Locate every Plasmodium parasite.
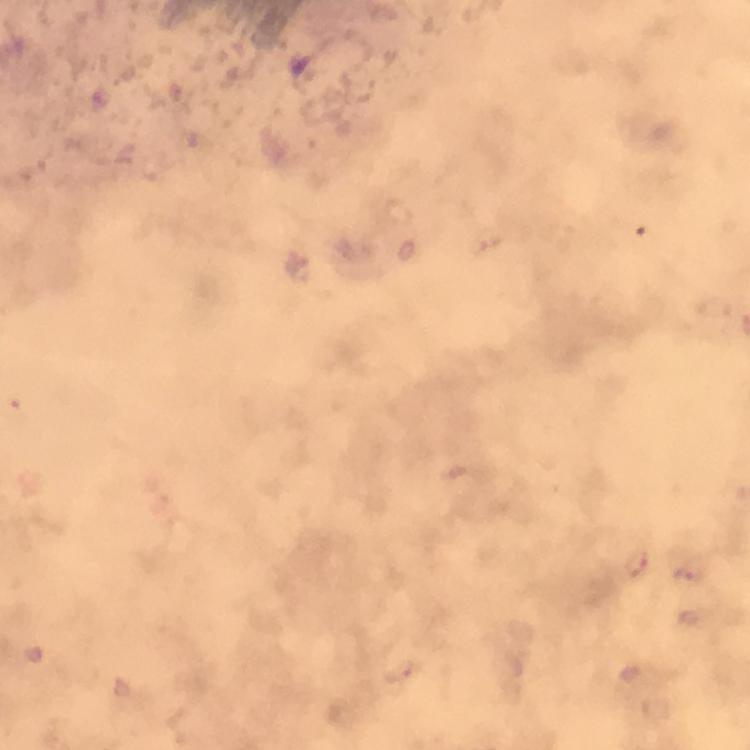

Approximate centers as (x, y) in pixels.
Plasmodium parasites: (689, 572).

context = from a diagnostic examination for malaria
stain = Giemsa
image size = 750×750 pixels
immersion oil = used
cropped from = a single field of view
magnification = 100x
preparation = thick smear
capture = smartphone photograph through a microscope